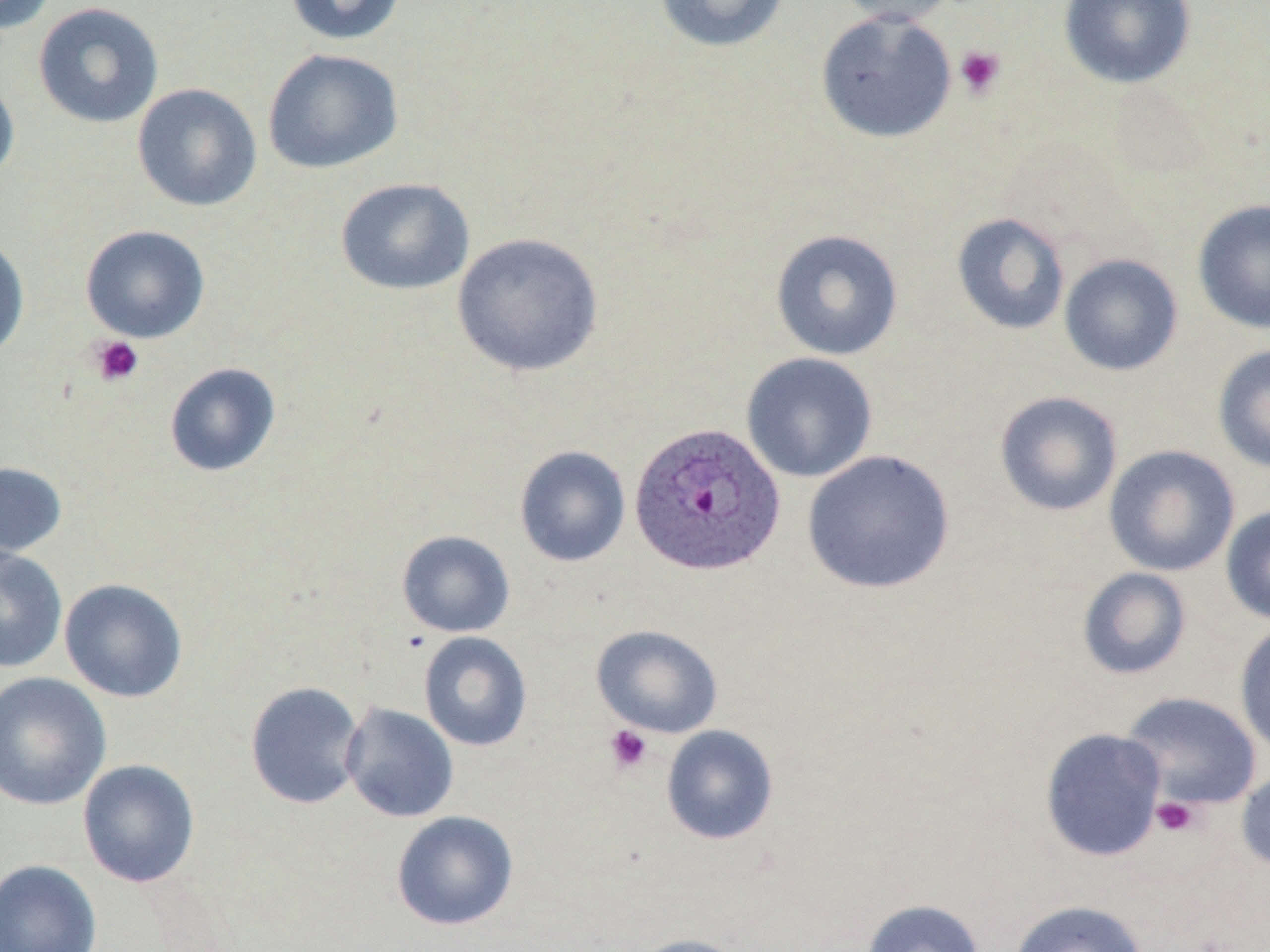
slide-level diagnosis = Plasmodium ovale
preparation = thin blood film
field of view = one of a larger specimen
image size = 1270×952 pixels
platelet locations = approximate bounding boxes as named x1/y1/x2/y2 corners in pixels: (x1=954, y1=45, x2=1006, y2=99), (x1=89, y1=335, x2=144, y2=387), (x1=604, y1=724, x2=653, y2=773), (x1=1150, y1=796, x2=1201, y2=838)
magnification = 1000x
modality = light microscopy
uninfected red blood cell locations = approximate bounding boxes as named x1/y1/x2/y2 corners in pixels: (x1=0, y1=0, x2=56, y2=34), (x1=284, y1=0, x2=407, y2=46), (x1=654, y1=0, x2=790, y2=53), (x1=830, y1=0, x2=961, y2=26), (x1=1059, y1=0, x2=1196, y2=89), (x1=33, y1=1, x2=164, y2=129), (x1=815, y1=9, x2=957, y2=143), (x1=262, y1=48, x2=404, y2=174), (x1=0, y1=74, x2=19, y2=186), (x1=132, y1=83, x2=262, y2=212), (x1=335, y1=177, x2=474, y2=296), (x1=1192, y1=199, x2=1270, y2=334), (x1=951, y1=212, x2=1071, y2=335), (x1=80, y1=224, x2=210, y2=343), (x1=770, y1=228, x2=904, y2=361), (x1=452, y1=232, x2=604, y2=377), (x1=0, y1=235, x2=30, y2=360), (x1=1059, y1=254, x2=1183, y2=376), (x1=1212, y1=343, x2=1270, y2=473), (x1=741, y1=352, x2=878, y2=483), (x1=164, y1=362, x2=281, y2=477), (x1=994, y1=390, x2=1123, y2=517), (x1=1104, y1=444, x2=1240, y2=577), (x1=514, y1=445, x2=631, y2=568), (x1=802, y1=449, x2=955, y2=594), (x1=0, y1=461, x2=68, y2=561), (x1=1220, y1=504, x2=1270, y2=626), (x1=396, y1=530, x2=516, y2=638), (x1=0, y1=547, x2=67, y2=673), (x1=1077, y1=567, x2=1192, y2=680), (x1=59, y1=578, x2=188, y2=703), (x1=1234, y1=621, x2=1270, y2=758), (x1=591, y1=624, x2=723, y2=738), (x1=419, y1=631, x2=532, y2=751), (x1=0, y1=671, x2=112, y2=811), (x1=244, y1=681, x2=366, y2=810), (x1=1120, y1=691, x2=1262, y2=811), (x1=340, y1=702, x2=459, y2=822), (x1=660, y1=724, x2=779, y2=845), (x1=1039, y1=727, x2=1167, y2=862), (x1=77, y1=758, x2=200, y2=888), (x1=1236, y1=767, x2=1270, y2=873), (x1=390, y1=810, x2=519, y2=931), (x1=0, y1=859, x2=101, y2=952), (x1=861, y1=898, x2=986, y2=952), (x1=1008, y1=899, x2=1149, y2=952), (x1=630, y1=933, x2=752, y2=952)
stain = May-Grünwald-Giemsa
Plasmodium ovale-infected red blood cell locations = approximate bounding boxes as named x1/y1/x2/y2 corners in pixels: (x1=628, y1=420, x2=786, y2=576)